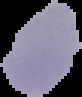
preparation = thin blood smear
image type = segmented cell region on a black background
image size = 82×97 pixels
result = negative for malaria parasites